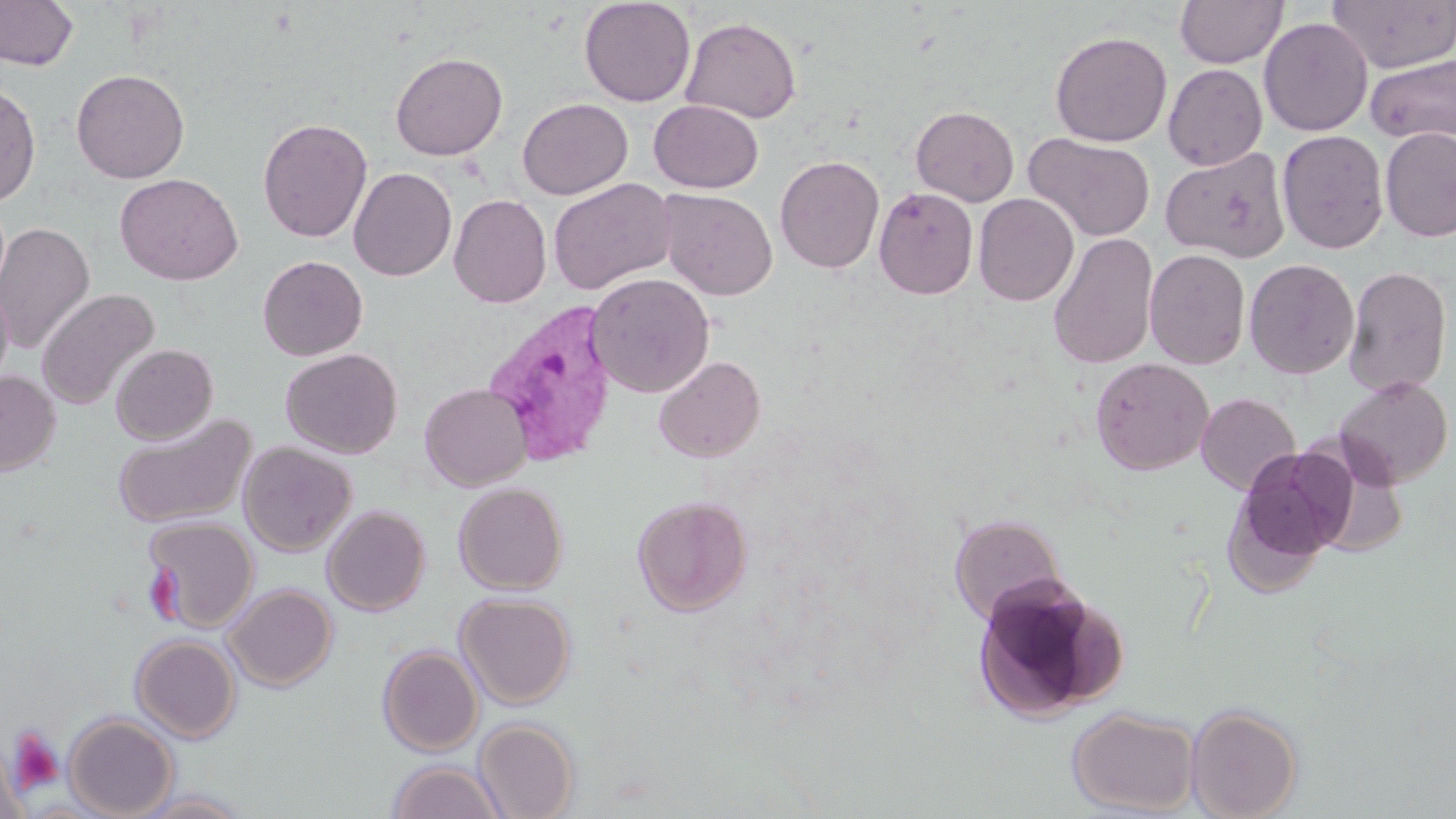

slide-level diagnosis = Plasmodium vivax
magnification = 1000x
preparation = thin blood film
stain = May-Grünwald-Giemsa
Plasmodium vivax-infected red blood cell locations = approximate bounding boxes as (x1, y1, x2, y2) in pixels: (481, 299, 620, 469)
image size = 1456×819 pixels
uninfected red blood cell locations = approximate bounding boxes as (x1, y1, x2, y2) in pixels: (0, 0, 79, 71), (579, 0, 696, 107), (1174, 0, 1288, 68), (1326, 0, 1456, 74), (681, 16, 802, 124), (1259, 17, 1373, 136), (1050, 30, 1172, 147), (390, 52, 508, 160), (1365, 54, 1456, 144), (1163, 64, 1267, 170), (71, 69, 190, 183), (0, 81, 41, 207), (518, 97, 633, 199), (649, 99, 763, 193), (910, 105, 1019, 206), (258, 117, 372, 243), (1380, 127, 1456, 242), (1277, 129, 1389, 254), (1023, 132, 1155, 242), (1161, 147, 1290, 262), (775, 155, 884, 273), (349, 167, 457, 281), (115, 173, 243, 284), (548, 178, 676, 295), (874, 186, 979, 299), (657, 188, 777, 300), (973, 193, 1079, 306), (449, 194, 552, 307), (0, 222, 95, 354), (1047, 232, 1159, 370), (1144, 249, 1250, 370), (257, 255, 368, 361), (1244, 258, 1359, 379), (1344, 266, 1452, 397), (586, 272, 715, 398), (0, 280, 14, 390), (37, 288, 159, 411), (110, 344, 218, 444), (280, 348, 403, 459), (654, 355, 766, 462), (1090, 356, 1214, 475), (0, 370, 60, 476), (1334, 375, 1453, 488), (419, 383, 532, 491), (1196, 392, 1300, 494), (112, 413, 256, 529), (238, 440, 357, 556), (1229, 444, 1359, 575), (453, 482, 568, 594), (632, 495, 752, 616), (321, 505, 431, 616), (949, 513, 1066, 626), (142, 516, 259, 632), (970, 577, 1122, 722), (223, 584, 337, 691), (455, 592, 576, 709), (131, 634, 241, 743), (377, 645, 483, 757), (1186, 703, 1302, 819), (1068, 707, 1200, 816), (63, 713, 178, 819), (473, 718, 579, 819), (0, 740, 29, 819), (385, 760, 507, 819), (129, 789, 250, 818)
field of view = one of a larger specimen
modality = optical microscopy
platelet locations = approximate bounding boxes as (x1, y1, x2, y2) in pixels: (6, 725, 65, 792)